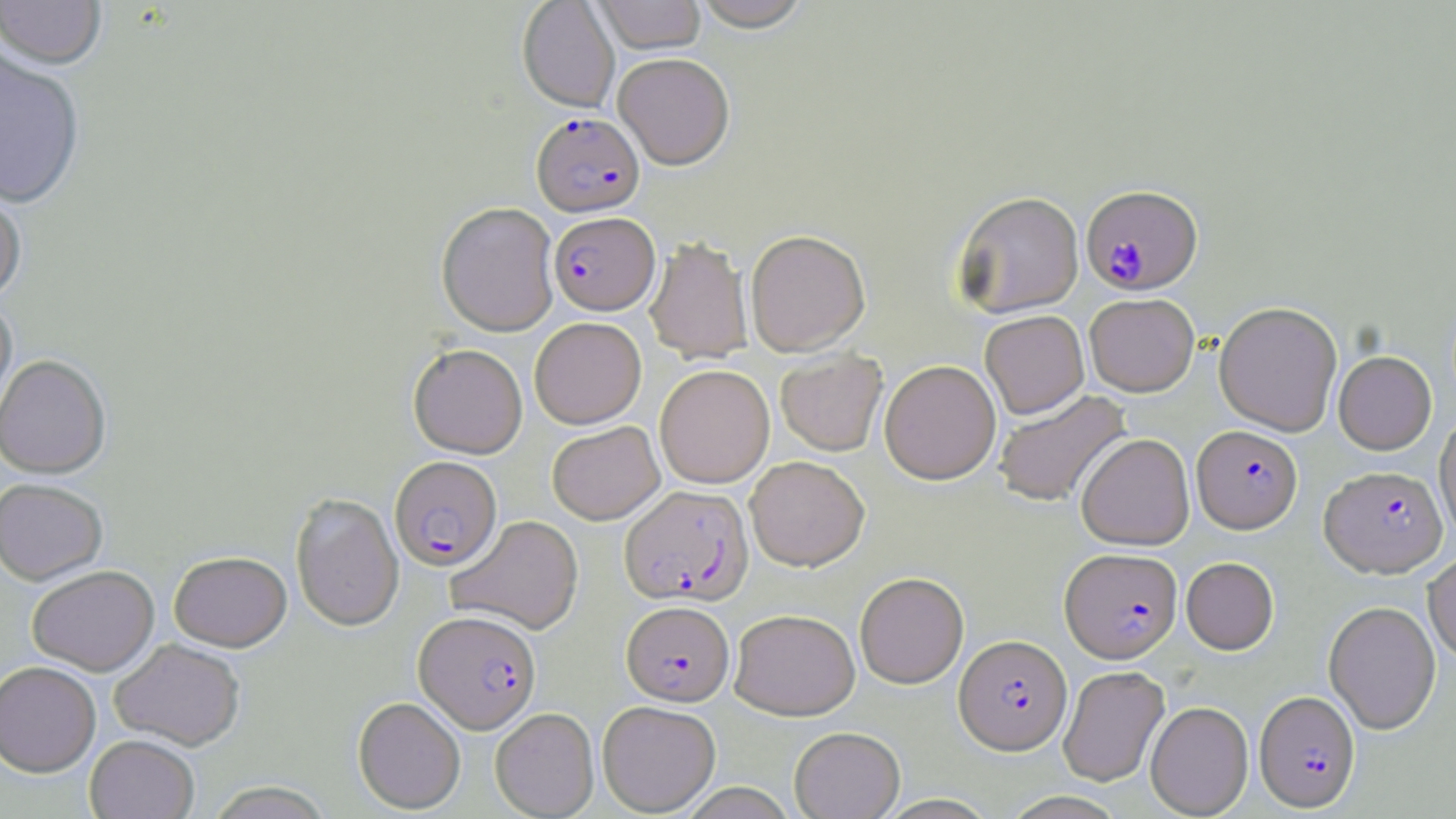 Approximate bounding boxes as (x1,y1)-(x2,y2) corner pairs in pixels. Plasmodium falciparum-infected red blood cell locations: (532,112)-(644,217), (1081,185)-(1203,295), (549,211)-(659,315), (1192,425)-(1302,532), (390,455)-(502,571), (1320,465)-(1447,577), (620,484)-(753,605), (1060,548)-(1182,662), (621,600)-(734,705), (414,609)-(541,733), (954,634)-(1072,754), (1253,690)-(1360,811). Uninfected red blood cell locations: (0,0)-(107,72), (517,0)-(619,113), (594,0)-(706,54), (692,0)-(813,32), (0,51)-(86,210), (614,53)-(734,169), (0,181)-(27,305), (953,191)-(1084,318), (436,202)-(559,336), (745,229)-(870,356), (645,236)-(752,363), (1084,293)-(1199,396), (0,298)-(17,431), (1214,301)-(1343,436), (980,310)-(1089,419), (529,317)-(646,429), (408,344)-(528,458), (775,350)-(888,456), (1333,351)-(1436,454), (0,355)-(111,479), (879,359)-(1001,484), (655,364)-(775,488), (994,390)-(1131,508), (1435,412)-(1456,543), (547,421)-(664,524), (1076,433)-(1195,550), (745,455)-(869,571), (0,478)-(108,586), (290,492)-(404,631), (446,514)-(584,634), (1423,550)-(1456,664), (169,551)-(291,651), (1181,556)-(1279,654), (27,565)-(159,676), (855,571)-(968,688), (1324,600)-(1441,734), (730,608)-(860,720), (109,638)-(246,750), (0,661)-(101,777), (1058,665)-(1170,787), (353,696)-(466,814), (597,700)-(720,816), (1145,701)-(1253,818), (490,708)-(599,818), (789,726)-(904,819), (85,735)-(199,819), (205,781)-(335,819), (677,783)-(799,818), (1000,790)-(1130,819). Slide-level diagnosis: Plasmodium falciparum. 1000x magnification. Optical microscopy. May-Grünwald-Giemsa-stained preparation. Image is 1456×819 pixels. One field of a larger specimen. Thin blood smear.